Name the parasite shown.
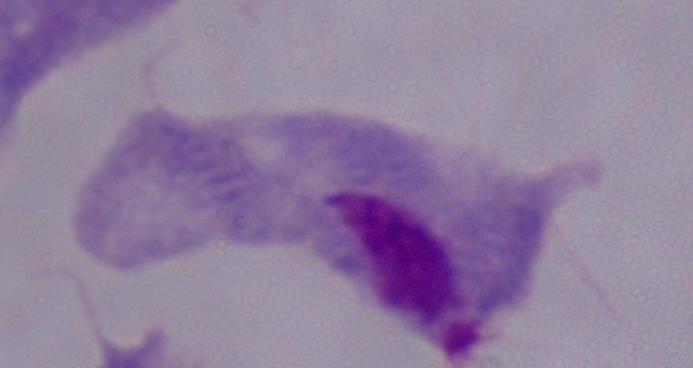
A trichomonad.

magnification: 1000x
modality: photomicrograph